Evaluate for malaria.
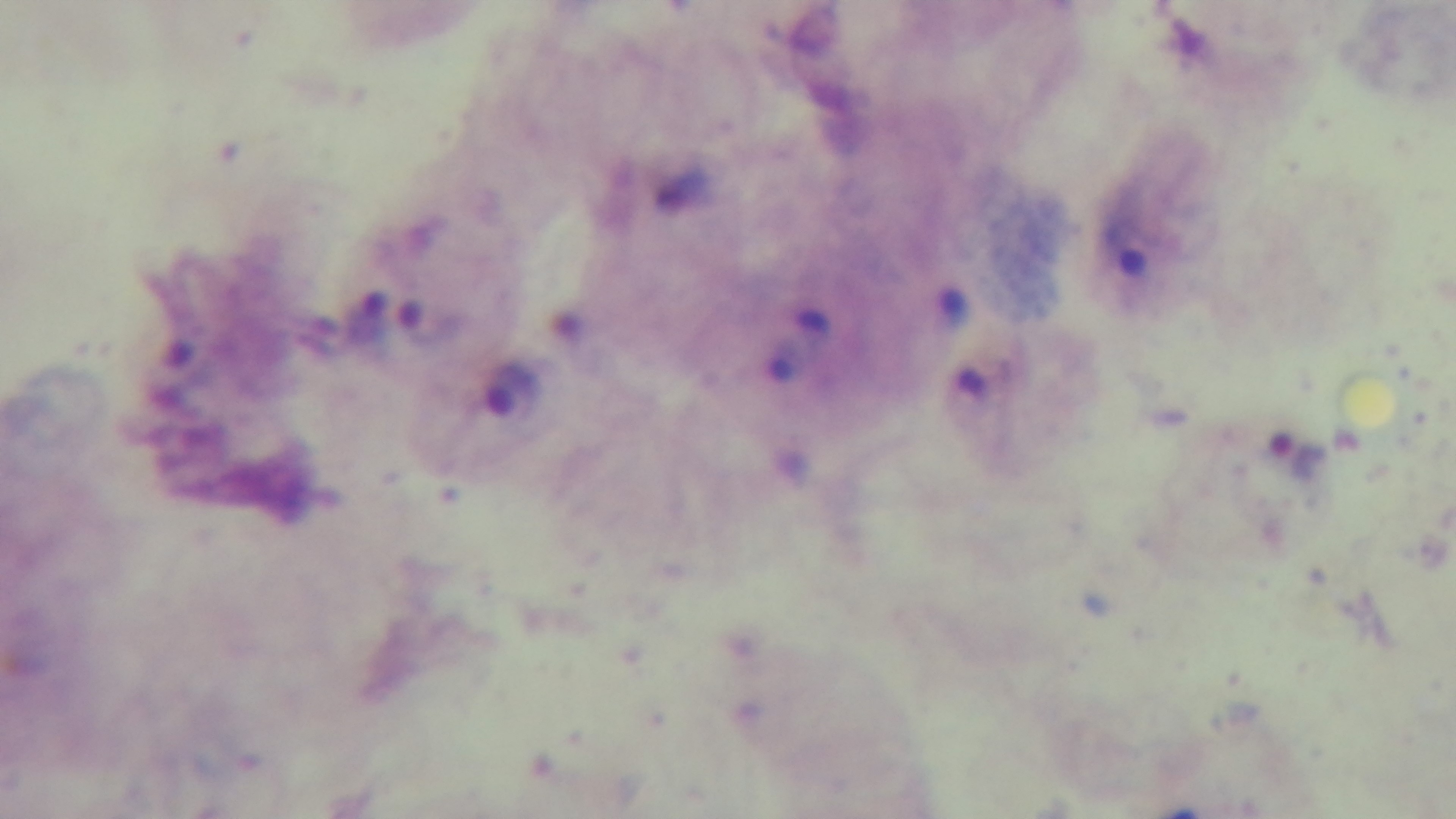
Positive.

Summary:
  - Capture: mounted 4K digital camera
  - Preparation: thick smear
  - Modality: light microscopy
  - Stain: Giemsa
  - Objective: 100x oil immersion
  - Field of view: single